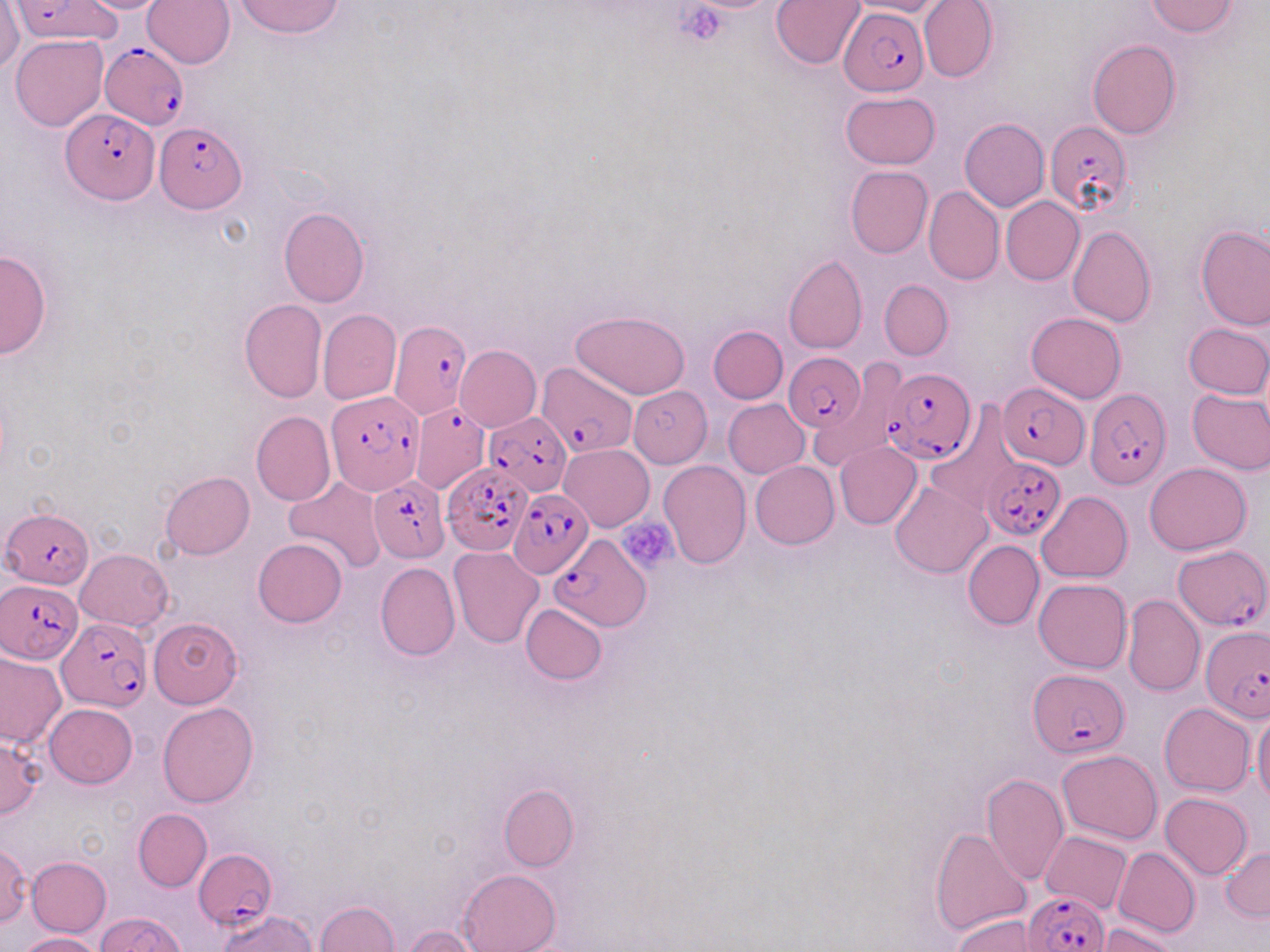

slide-level diagnosis = Plasmodium falciparum
platelet locations = approximate bounding boxes as (x1,y1)-(x2,y2) corner pairs in pixels: (673,4)-(727,44), (616,517)-(677,573)
modality = optical microscopy
Plasmodium falciparum-infected red blood cell locations = approximate bounding boxes as (x1,y1)-(x2,y2) corner pairs in pixels: (10,0)-(119,43), (840,7)-(928,95), (100,43)-(189,130), (62,106)-(157,204), (1044,121)-(1132,216), (155,122)-(247,215), (388,321)-(474,422), (784,353)-(865,434), (537,362)-(638,456), (881,367)-(976,463), (998,383)-(1089,469), (1085,387)-(1171,488), (326,390)-(425,496), (410,401)-(492,493), (484,411)-(572,494), (983,457)-(1066,540), (443,462)-(531,556), (368,474)-(449,561), (509,489)-(593,579), (3,506)-(93,590), (550,533)-(649,631), (1173,543)-(1270,631), (1,578)-(84,663), (57,618)-(150,713), (1202,624)-(1268,719), (1028,670)-(1129,759), (195,849)-(277,931), (1024,889)-(1109,952)
preparation = thin blood smear
field of view = one of a larger specimen
image size = 1270×952 pixels
uninfected red blood cell locations = approximate bounding boxes as (x1,y1)-(x2,y2) corner pairs in pixels: (71,0)-(175,13), (234,0)-(344,38), (844,0)-(948,17), (919,0)-(999,83), (0,1)-(23,76), (141,1)-(235,69), (771,1)-(866,69), (1144,1)-(1239,37), (11,35)-(108,131), (1087,39)-(1181,139), (840,91)-(941,169), (959,118)-(1050,210), (845,165)-(934,259), (923,186)-(1004,285), (1002,197)-(1084,285), (278,207)-(369,308), (1195,224)-(1270,331), (1069,226)-(1156,326), (0,248)-(52,360), (783,254)-(868,354), (879,280)-(953,361), (240,300)-(327,403), (318,309)-(401,404), (570,310)-(691,398), (1026,312)-(1126,403), (1184,323)-(1269,399), (709,325)-(788,404), (454,345)-(540,432), (626,385)-(707,466), (1187,389)-(1270,475), (734,397)-(820,545), (723,399)-(809,478), (926,406)-(1020,519), (251,410)-(335,506), (834,442)-(921,529), (560,444)-(654,531), (659,460)-(751,567), (751,461)-(840,548), (1144,463)-(1252,554), (160,471)-(254,560), (284,476)-(387,574), (891,480)-(990,578), (1037,491)-(1133,582), (253,538)-(347,627), (963,539)-(1044,629), (76,548)-(172,631), (449,548)-(545,648), (375,562)-(460,661), (1035,579)-(1132,673), (1123,595)-(1204,696), (520,604)-(607,685), (149,617)-(243,707), (0,650)-(65,749), (1160,702)-(1254,796), (44,703)-(137,788), (158,703)-(259,807), (1253,706)-(1270,808), (0,734)-(45,820), (1056,749)-(1163,844), (981,773)-(1069,886), (498,783)-(577,873), (1160,794)-(1252,879), (133,809)-(212,891), (930,826)-(1030,936), (1040,831)-(1132,913), (0,841)-(31,927), (1112,847)-(1200,938), (1222,847)-(1270,921), (25,856)-(110,937), (457,868)-(560,952), (314,902)-(400,952), (218,910)-(317,952), (95,912)-(187,952), (951,913)-(1045,952), (1099,922)-(1183,952), (401,926)-(485,952), (16,932)-(103,951)
magnification = 1000x
stain = May-Grünwald-Giemsa